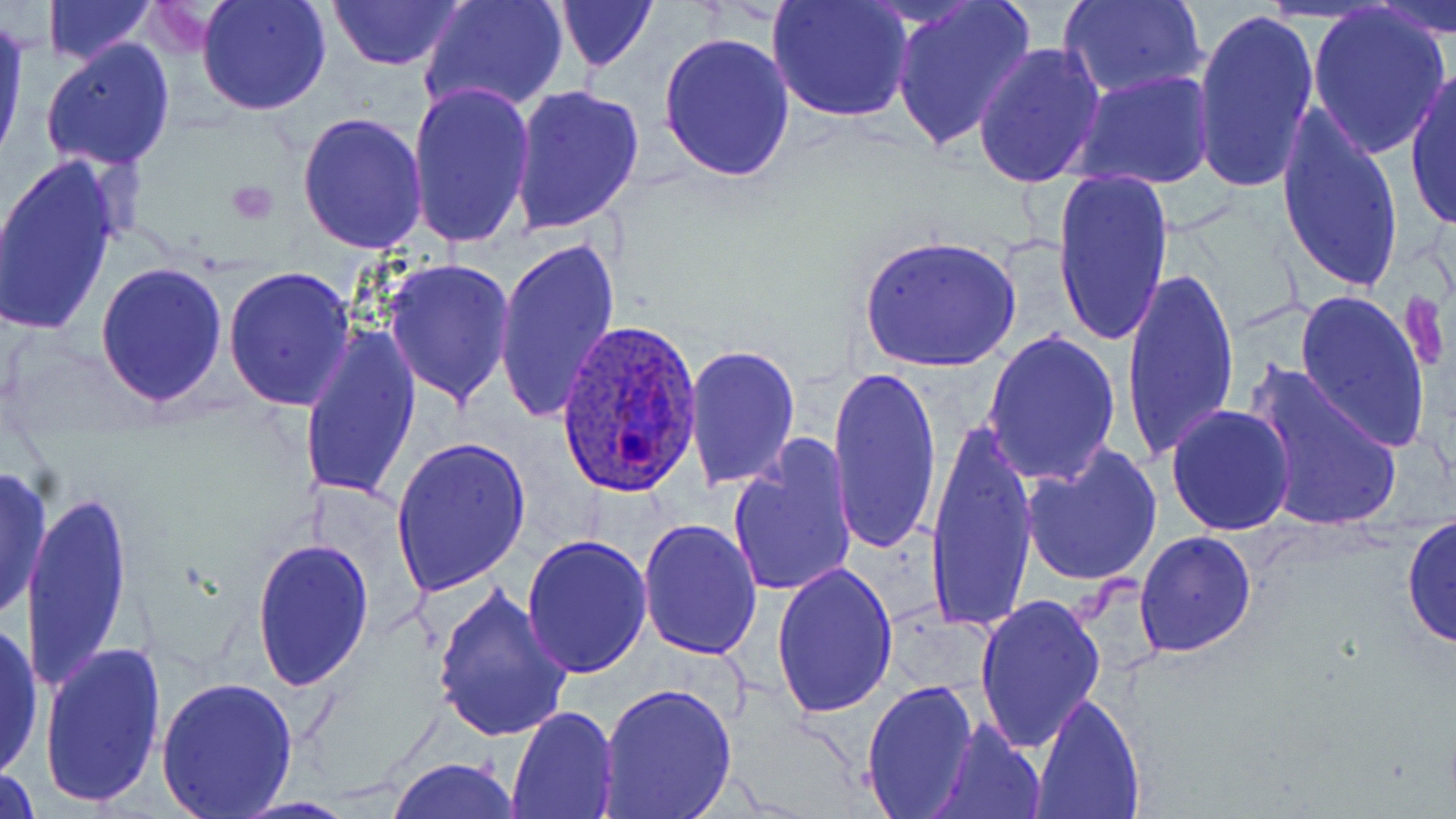 Approximate bounding boxes as (x1,y1)-(x2,y2) corner pairs in pixels. Uninfected red blood cell locations (subset): (42,0)-(155,65), (195,0)-(332,117), (327,0)-(467,70), (421,0)-(569,117), (554,0)-(658,73), (767,0)-(915,124), (890,0)-(1037,151), (1061,0)-(1208,100), (1369,0)-(1454,43), (1307,4)-(1453,157), (1191,7)-(1320,192), (0,15)-(28,166), (659,33)-(796,181), (41,38)-(176,172), (972,43)-(1107,189), (1404,66)-(1456,231), (1074,70)-(1216,191), (405,80)-(535,251), (507,85)-(644,237), (1274,103)-(1405,298), (297,112)-(429,253), (0,155)-(126,337), (1051,169)-(1173,347), (494,234)-(621,428), (382,258)-(515,407), (95,262)-(227,407), (1121,262)-(1239,469), (222,267)-(357,411), (1293,289)-(1431,453), (299,319)-(422,505), (982,329)-(1120,486), (683,342)-(800,491), (1244,358)-(1403,535), (827,362)-(941,556), (1167,404)-(1296,537), (923,415)-(1039,642), (391,435)-(531,597), (727,437)-(858,599), (1020,444)-(1163,588), (0,466)-(51,621), (18,490)-(135,693), (1402,513)-(1456,654), (638,516)-(763,658), (1134,531)-(1256,657), (521,534)-(653,678), (251,538)-(375,691), (769,558)-(897,719), (429,585)-(573,743), (976,593)-(1106,753), (0,618)-(45,782), (38,640)-(168,808), (157,675)-(298,815), (861,680)-(978,816), (598,681)-(738,818), (1030,694)-(1145,818), (506,706)-(618,817), (929,719)-(1046,819), (388,757)-(523,818), (0,766)-(40,816), (231,797)-(356,817). Platelet locations: (227,181)-(276,224), (1401,289)-(1447,372). Plasmodium ovale-infected red blood cell locations (subset): (555,315)-(705,496). Slide-level diagnosis: Plasmodium ovale. Image is 1456×819 pixels. Captured at 1000x magnification. One field of a larger specimen. Thin blood film. Light microscopy. May-Grünwald-Giemsa-stained preparation.